Assess this cell for malaria.
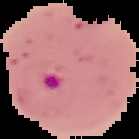
It is parasitized.

image size = 139×139 pixels
image type = segmented cell region with the area outside set to black
preparation = thin blood film